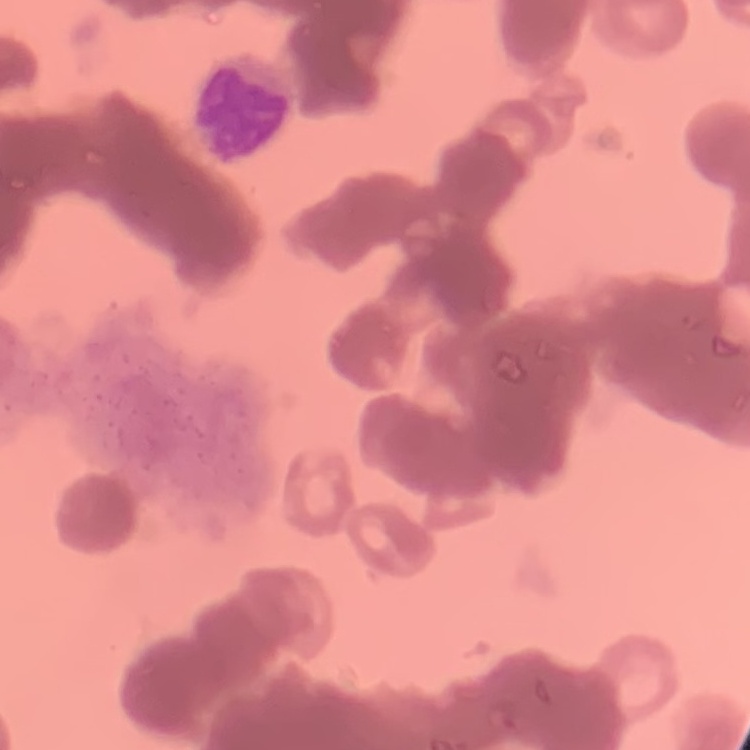 The erythrocytes exhibit rouleaux formation. Thin peripheral smear. Field's or Giemsa stain. Square crop of a larger photomicrograph.